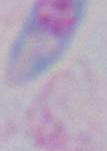 Toxoplasma gondii is shown. Micrograph. 1000x magnification.